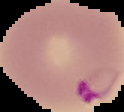

Result: Plasmodium parasites detected. From a thin blood smear. Image is 124×112 pixels. Segmented cell region on a black background.